State which cell type is depicted.
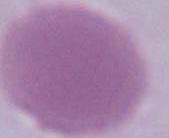
This is an erythrocyte.

Micrograph. Captured at 1000x magnification.